Assess this cell for malaria.
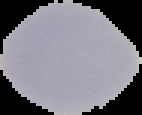

It is uninfected.

Summary:
  - Preparation: thin blood smear
  - Image type: segmented cell region on a black background
  - Image size: 142×115 pixels